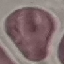 Malaria status: uninfected. Thin blood smear. Cell patch, automatically extracted from a larger field of view and resized to 64 × 64 pixels. Photographed with a smartphone camera at the microscope eyepiece. Giemsa-stained preparation.